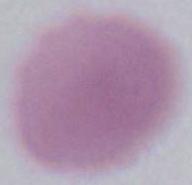

A red blood cell is shown. 1000x magnification. Micrograph.